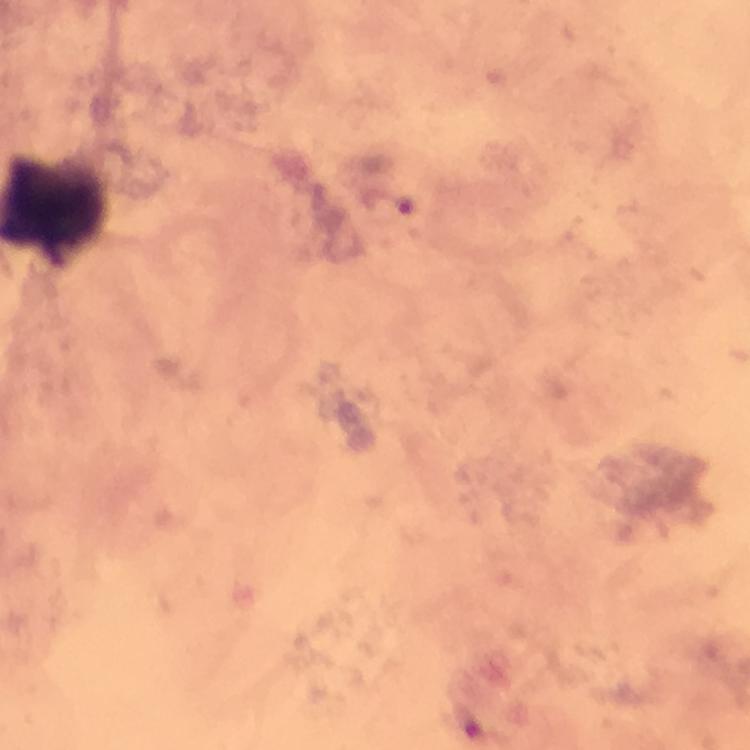

Approximate centers as {x, y} in pixels. Malaria parasite locations: {405, 207}. Image is 750×750 pixels. Giemsa stain. Immersion oil applied. Thick blood smear. 100x magnification. A crop from one field of view. From a diagnostic examination for malaria. Smartphone photograph taken through a microscope.